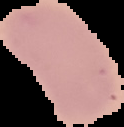
Summary:
  - Image type: segmented cell region with the area outside set to black
  - Image size: 124×127 pixels
  - Result: negative for Plasmodium parasites
  - Preparation: thin blood smear